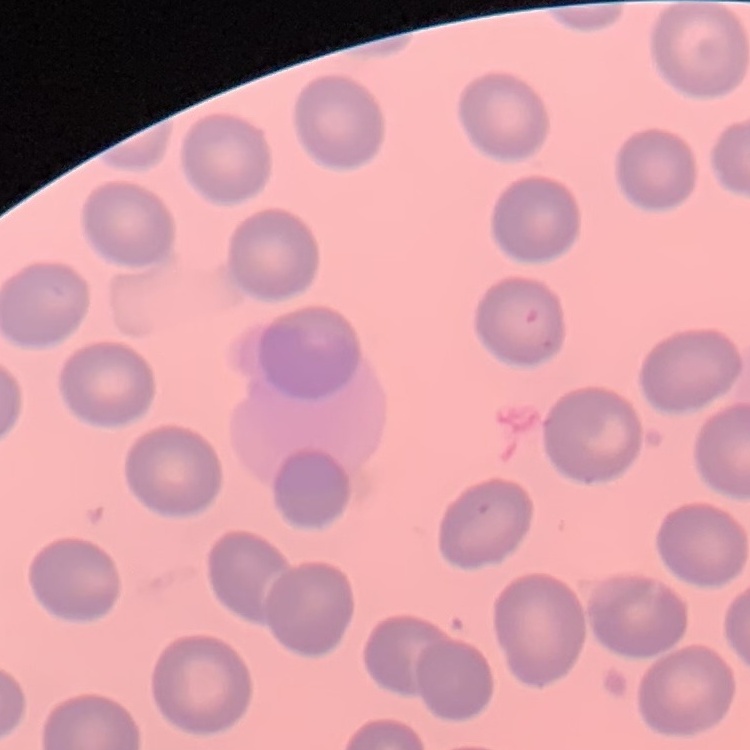 The red blood cells exhibit no rouleaux formation. Thin blood smear. One tile cut from a larger photomicrograph. Field's or Giemsa stain.